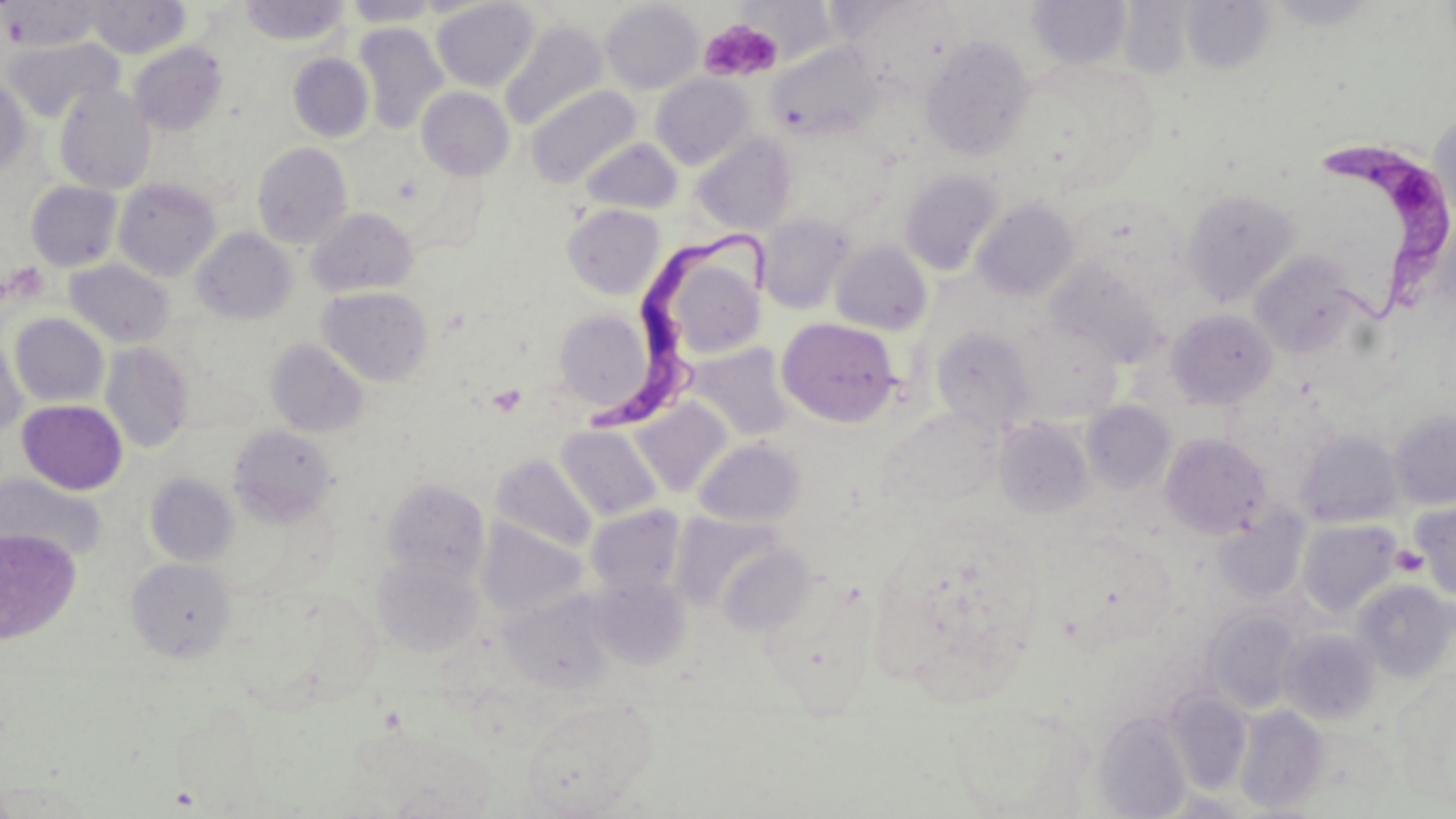
Approximate bounding boxes as (x1, y1, x2, y2) in pixels. Platelet locations: (699, 19, 783, 83), (1390, 545, 1428, 577). Uninfected red blood cell locations: (84, 0, 190, 58), (239, 0, 349, 45), (1264, 0, 1383, 30), (3, 1, 102, 50), (342, 1, 443, 26), (431, 1, 540, 91), (1026, 1, 1133, 69), (601, 2, 704, 94), (1182, 2, 1276, 74), (740, 3, 838, 64), (500, 20, 608, 131), (354, 22, 448, 134), (920, 36, 1036, 160), (3, 38, 122, 123), (765, 40, 882, 141), (129, 42, 227, 135), (288, 53, 374, 142), (1010, 56, 1160, 196), (651, 73, 756, 169), (0, 76, 31, 175), (55, 83, 157, 194), (527, 85, 638, 187), (417, 87, 514, 180), (1430, 116, 1456, 230), (692, 133, 797, 234), (581, 137, 683, 214), (251, 141, 352, 249), (900, 170, 1003, 275), (113, 178, 220, 281), (26, 181, 123, 271), (1182, 189, 1299, 304), (1071, 193, 1186, 293), (972, 199, 1079, 301), (562, 204, 664, 299), (307, 207, 418, 297), (758, 214, 855, 314), (192, 228, 295, 324), (648, 238, 767, 364), (830, 240, 932, 336), (1249, 251, 1361, 358), (65, 259, 175, 349), (1046, 262, 1164, 368), (318, 286, 433, 386), (554, 308, 656, 413), (1167, 309, 1277, 409), (10, 313, 108, 407), (777, 318, 900, 426), (1013, 318, 1123, 422), (932, 326, 1036, 433), (0, 331, 27, 442), (266, 339, 368, 437), (100, 342, 194, 453), (686, 342, 796, 442), (17, 400, 128, 495), (629, 400, 733, 498), (1081, 401, 1175, 494), (1389, 408, 1456, 509), (995, 417, 1095, 519), (228, 425, 337, 526), (556, 425, 663, 521), (1294, 428, 1404, 528), (1160, 433, 1271, 539), (694, 438, 806, 528), (492, 454, 596, 554), (146, 472, 238, 566), (1, 473, 106, 564), (381, 478, 489, 584), (1410, 501, 1456, 601), (585, 505, 687, 595), (1213, 508, 1311, 607), (1297, 518, 1403, 618), (477, 519, 586, 618), (1, 528, 81, 645), (716, 544, 816, 637), (372, 554, 483, 657), (127, 558, 236, 662), (757, 579, 879, 717), (1352, 579, 1455, 683), (501, 592, 615, 695), (1204, 609, 1303, 714), (1278, 628, 1382, 725), (1167, 691, 1252, 794), (519, 696, 659, 817), (1235, 705, 1329, 813), (1094, 712, 1192, 818), (0, 777, 96, 816). Trypanosoma brucei locations: (1298, 143, 1456, 317), (584, 229, 771, 431). Slide-level diagnosis: Trypanosoma brucei. Light microscopy. Image is 1456×819 pixels. Thin blood smear. One field of a larger specimen. 1000x magnification. May-Grünwald-Giemsa-stained preparation.